Identify the cell.
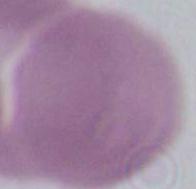
This is an erythrocyte.

Summary:
  - Magnification: 1000x
  - Modality: micrograph